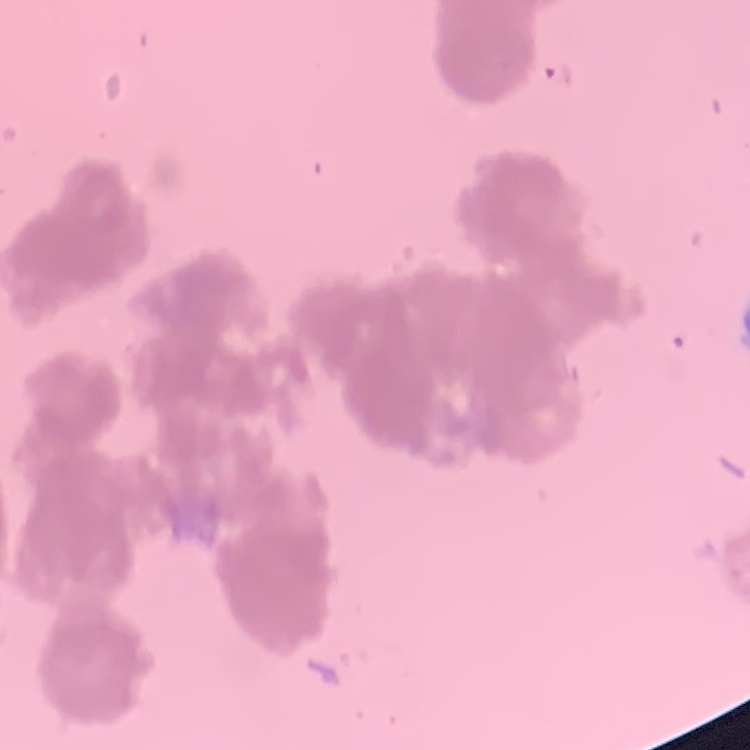
erythrocyte_morphology: rouleaux formation
image_type: one tile cut from a larger photomicrograph
preparation: thin peripheral smear
stain: Field's or Giemsa